Identify the cell.
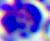
This is a leukocyte.

Photomicrograph. Captured at 400x magnification.